Locate and identify every blood parasite.
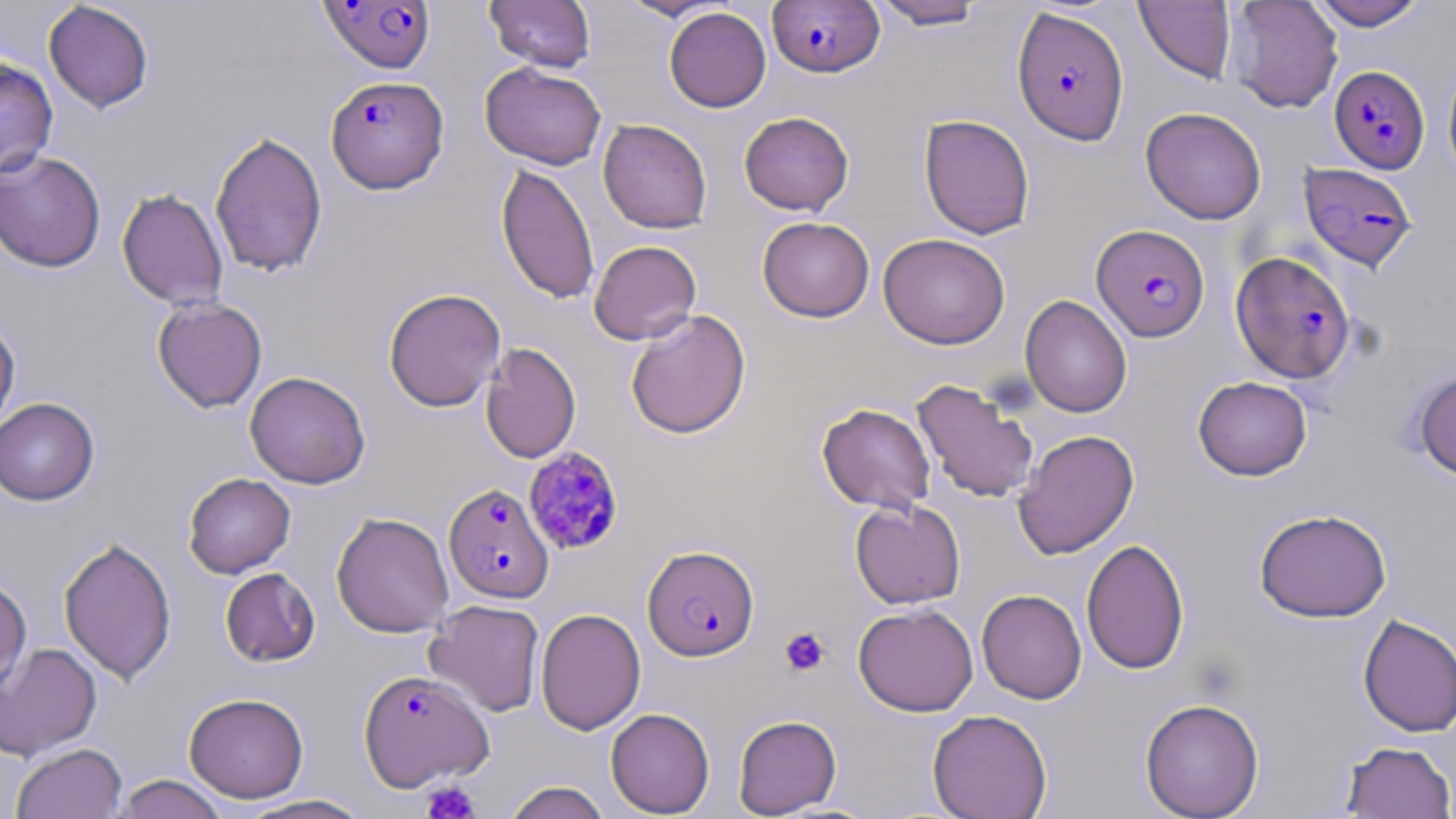
Approximate bounding boxes as (x1,y1)-(x2,y2) corner pairs in pixels.
Plasmodium falciparum-infected red blood cells: (318,1)-(437,74), (768,1)-(884,78), (1012,6)-(1129,145), (1329,64)-(1430,173), (326,74)-(450,194), (1298,162)-(1419,272), (1091,224)-(1210,342), (1231,251)-(1356,383), (523,447)-(625,555), (443,482)-(554,605), (643,544)-(759,661), (358,669)-(494,792).
No Plasmodium ovale, Plasmodium malariae, Plasmodium vivax, Babesia divergens, or Trypanosoma brucei observed.

slide-level diagnosis = Plasmodium falciparum
image size = 1456×819 pixels
preparation = thin blood film
platelet locations = approximate bounding boxes as (x1,y1)-(x2,y2) corner pairs in pixels: (779,626)-(830,677), (420,781)-(482,819)
magnification = 1000x
field of view = single
uninfected red blood cell locations = approximate bounding boxes as (x1,y1)-(x2,y2) corner pairs in pixels: (485,0)-(596,72), (617,0)-(731,21), (870,0)-(987,30), (1224,0)-(1343,114), (1309,0)-(1429,30), (43,1)-(155,113), (1134,1)-(1236,83), (664,7)-(771,112), (0,57)-(58,178), (1442,57)-(1456,186), (480,61)-(607,170), (1140,107)-(1266,225), (739,112)-(854,215), (918,114)-(1035,239), (598,119)-(712,233), (209,130)-(328,278), (0,150)-(107,273), (496,162)-(600,304), (116,188)-(229,310), (757,216)-(874,322), (878,233)-(1010,349), (589,240)-(701,345), (383,288)-(506,412), (1020,295)-(1133,417), (152,298)-(268,412), (625,310)-(751,439), (0,317)-(21,434), (480,342)-(581,463), (1411,367)-(1456,481), (244,371)-(371,489), (1193,376)-(1312,481), (911,378)-(1039,504), (0,397)-(99,505), (816,402)-(936,515), (1013,429)-(1140,560), (183,473)-(296,578), (850,499)-(966,609), (1254,509)-(1392,622), (331,512)-(454,638), (58,535)-(177,686), (1081,539)-(1189,675), (220,567)-(320,667), (0,575)-(32,698), (977,589)-(1087,704), (425,599)-(546,716), (853,603)-(979,716), (535,607)-(646,735), (1358,613)-(1456,737), (0,642)-(102,761), (184,692)-(309,803), (1139,697)-(1264,819), (605,708)-(715,817), (926,709)-(1053,819), (732,714)-(842,817), (1340,741)-(1456,818), (11,742)-(127,819), (112,774)-(230,819), (502,780)-(612,819), (235,794)-(374,818)
modality = light microscopy
stain = May-Grünwald-Giemsa